Name the parasite shown.
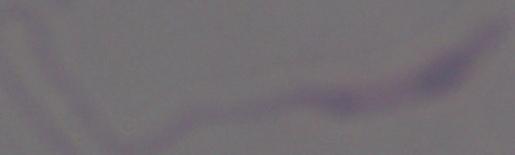
Leishmania.

Micrograph. 1000x magnification.